Identify the parasite.
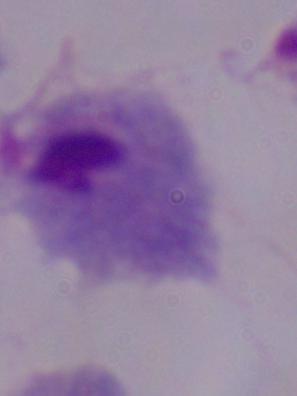
A trichomonad.

modality = photomicrograph
magnification = 1000x